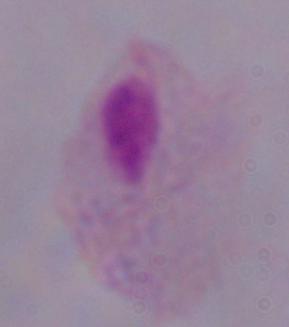
magnification: 1000x
identification: trichomonad
modality: photomicrograph